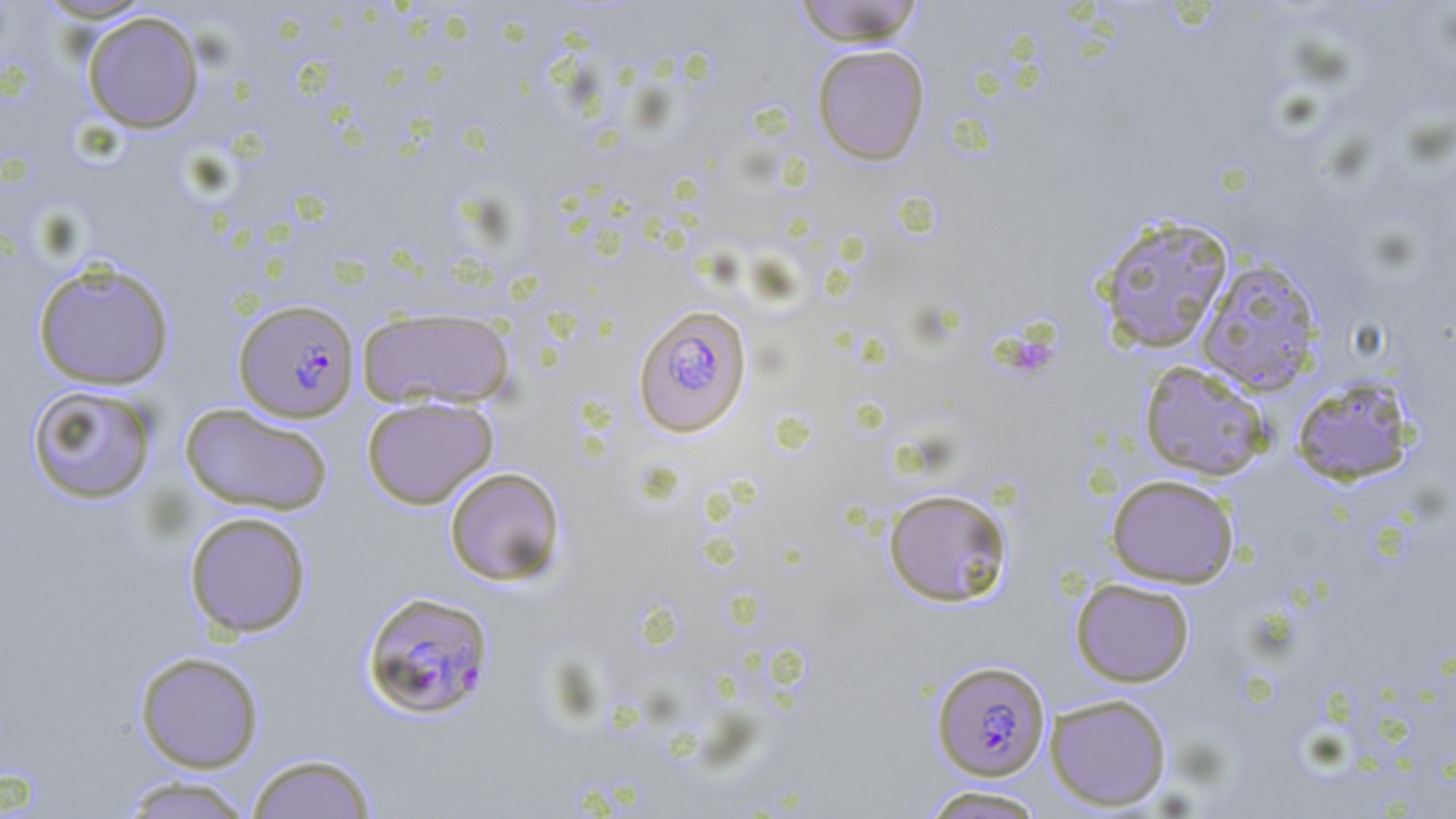
Approximate bounding boxes as named x1/y1/x2/y2 corners in pixels. Platelet locations: (x1=1016, y1=339, x2=1053, y2=376). Uninfected red blood cell locations: (x1=34, y1=0, x2=157, y2=23), (x1=791, y1=0, x2=925, y2=46), (x1=81, y1=11, x2=205, y2=133), (x1=811, y1=44, x2=930, y2=166), (x1=1095, y1=214, x2=1235, y2=354), (x1=1195, y1=258, x2=1324, y2=396), (x1=31, y1=260, x2=176, y2=391), (x1=356, y1=306, x2=517, y2=410), (x1=1138, y1=360, x2=1272, y2=481), (x1=1289, y1=375, x2=1417, y2=486), (x1=26, y1=384, x2=159, y2=504), (x1=361, y1=395, x2=499, y2=509), (x1=179, y1=403, x2=335, y2=516), (x1=444, y1=466, x2=566, y2=586), (x1=1106, y1=474, x2=1239, y2=588), (x1=882, y1=487, x2=1013, y2=607), (x1=183, y1=510, x2=312, y2=638), (x1=1070, y1=577, x2=1195, y2=688), (x1=134, y1=651, x2=265, y2=773), (x1=1044, y1=693, x2=1172, y2=812), (x1=245, y1=752, x2=379, y2=819), (x1=116, y1=775, x2=258, y2=819), (x1=918, y1=785, x2=1050, y2=818). Plasmodium falciparum-infected red blood cell locations: (x1=233, y1=298, x2=360, y2=422), (x1=632, y1=303, x2=753, y2=437), (x1=359, y1=589, x2=495, y2=721), (x1=931, y1=659, x2=1051, y2=781). Slide-level diagnosis: Plasmodium falciparum. Image is 1456×819 pixels. Thin blood film. Optical microscopy. May-Grünwald-Giemsa stain. One field of a larger specimen. Captured at 1000x magnification.